Assess this cell for malaria.
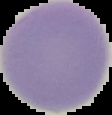
Uninfected.

Summary:
  - Image size: 112×115 pixels
  - Preparation: thin blood film
  - Image type: segmented cell region on a black background